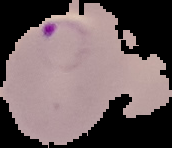

preparation: thin blood film
image_size: 172×148 pixels
result: malaria parasites identified
image_type: segmented cell region with the area outside set to black